Identify the cell.
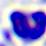

A leukocyte.

{
  "magnification": "400x",
  "modality": "micrograph"
}